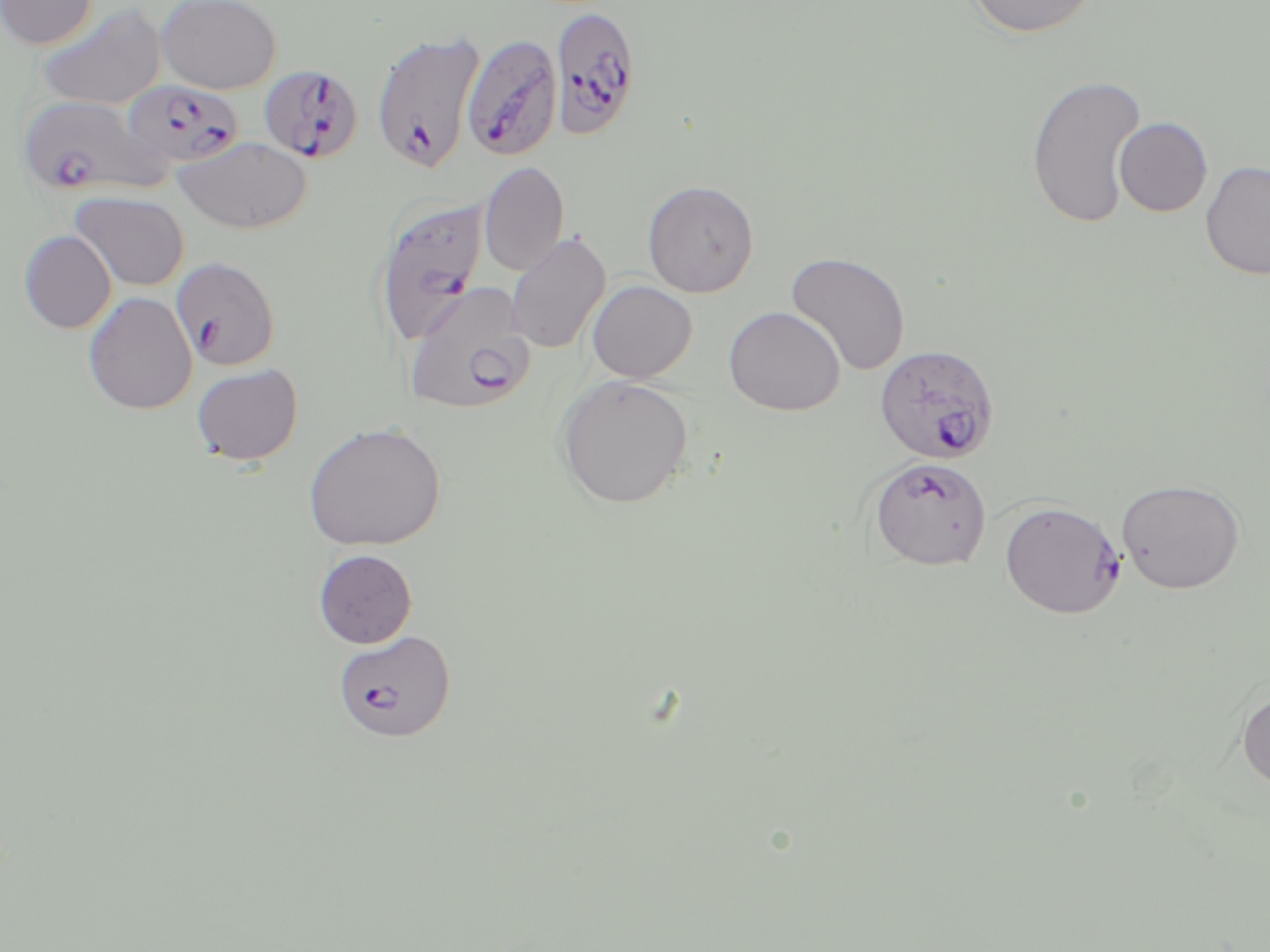
Approximate bounding boxes as (x1, y1, x2, y2) in pixels. Plasmodium falciparum-infected red blood cell locations: (554, 6, 646, 141), (371, 30, 485, 175), (472, 32, 567, 164), (258, 64, 364, 164), (121, 80, 242, 170), (18, 94, 167, 198), (373, 195, 490, 348), (171, 256, 279, 370), (403, 282, 536, 415), (875, 343, 1000, 464), (868, 456, 993, 571), (999, 499, 1126, 619), (333, 629, 457, 742). Uninfected red blood cell locations: (0, 0, 97, 50), (156, 0, 282, 94), (967, 0, 1099, 39), (35, 3, 166, 111), (1025, 73, 1146, 227), (1114, 117, 1213, 217), (174, 136, 312, 234), (479, 161, 569, 277), (1200, 161, 1270, 280), (642, 179, 759, 297), (70, 192, 190, 291), (19, 230, 116, 333), (505, 231, 611, 354), (785, 251, 911, 375), (586, 280, 697, 383), (83, 292, 197, 415), (724, 306, 845, 416), (191, 363, 303, 466), (555, 375, 693, 509), (302, 422, 446, 552), (1116, 478, 1246, 594), (313, 549, 417, 648), (1237, 688, 1270, 792). Slide-level diagnosis: Plasmodium falciparum. Image is 1270×952 pixels. 1000x magnification. Single field of view. Thin blood film. May-Grünwald-Giemsa-stained preparation. Light microscopy.